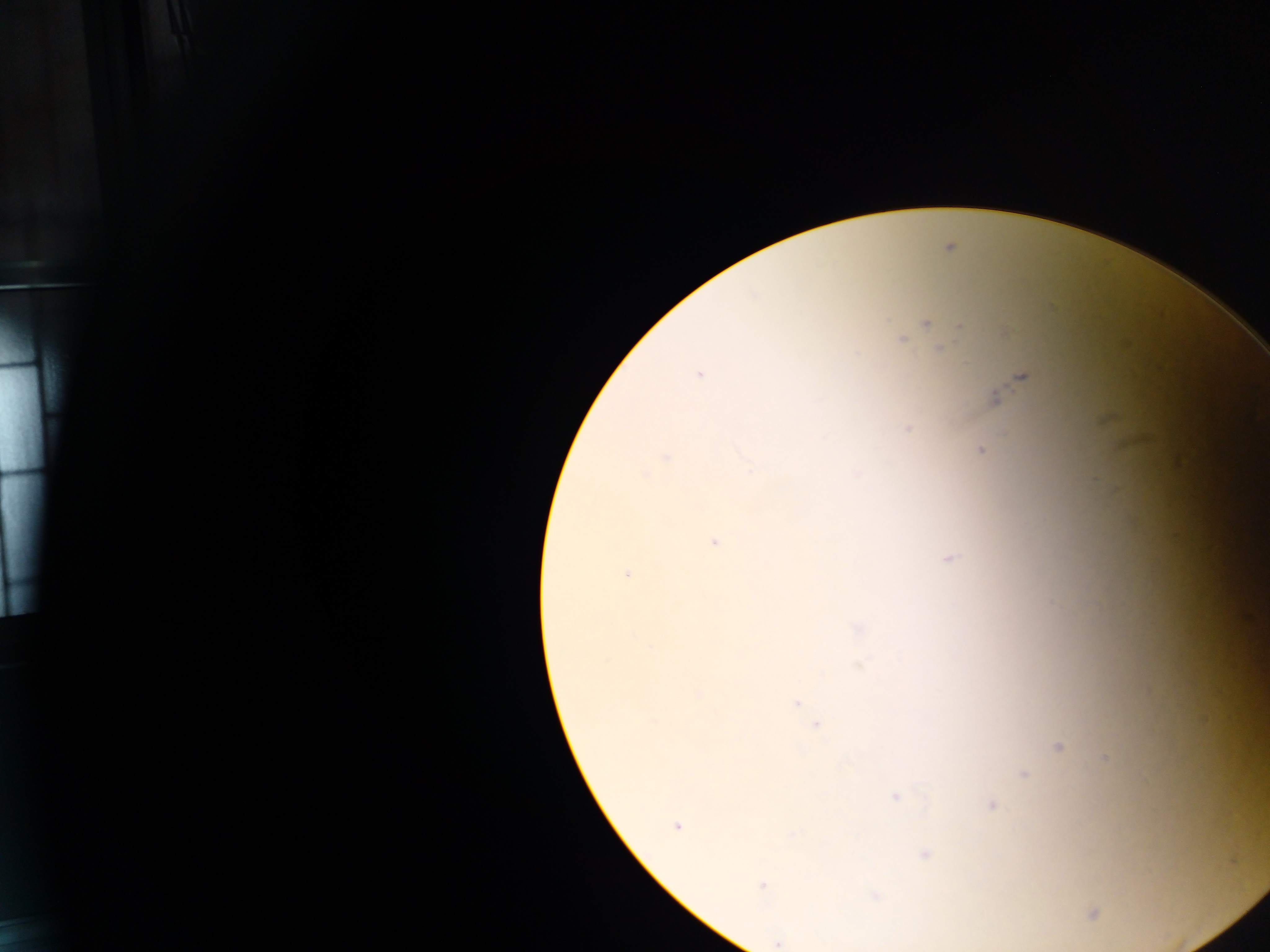

Approximate centers as (x, y) in pixels. Malaria parasite locations: (949, 248), (753, 295), (1053, 308), (926, 324), (959, 326), (1006, 333), (901, 341), (940, 349), (699, 374), (1022, 377), (995, 399), (907, 429), (981, 450), (666, 457), (645, 475), (715, 542), (950, 558), (628, 574), (857, 628), (797, 702), (816, 725), (1058, 746), (1105, 759), (1023, 773), (894, 796), (992, 804), (676, 826), (924, 854), (762, 886), (876, 896), (1093, 913), (778, 943). Thick blood smear. Image is 1270×952 pixels. One field of view. Mobile-phone photograph taken through the microscope. Sample from Ghana.